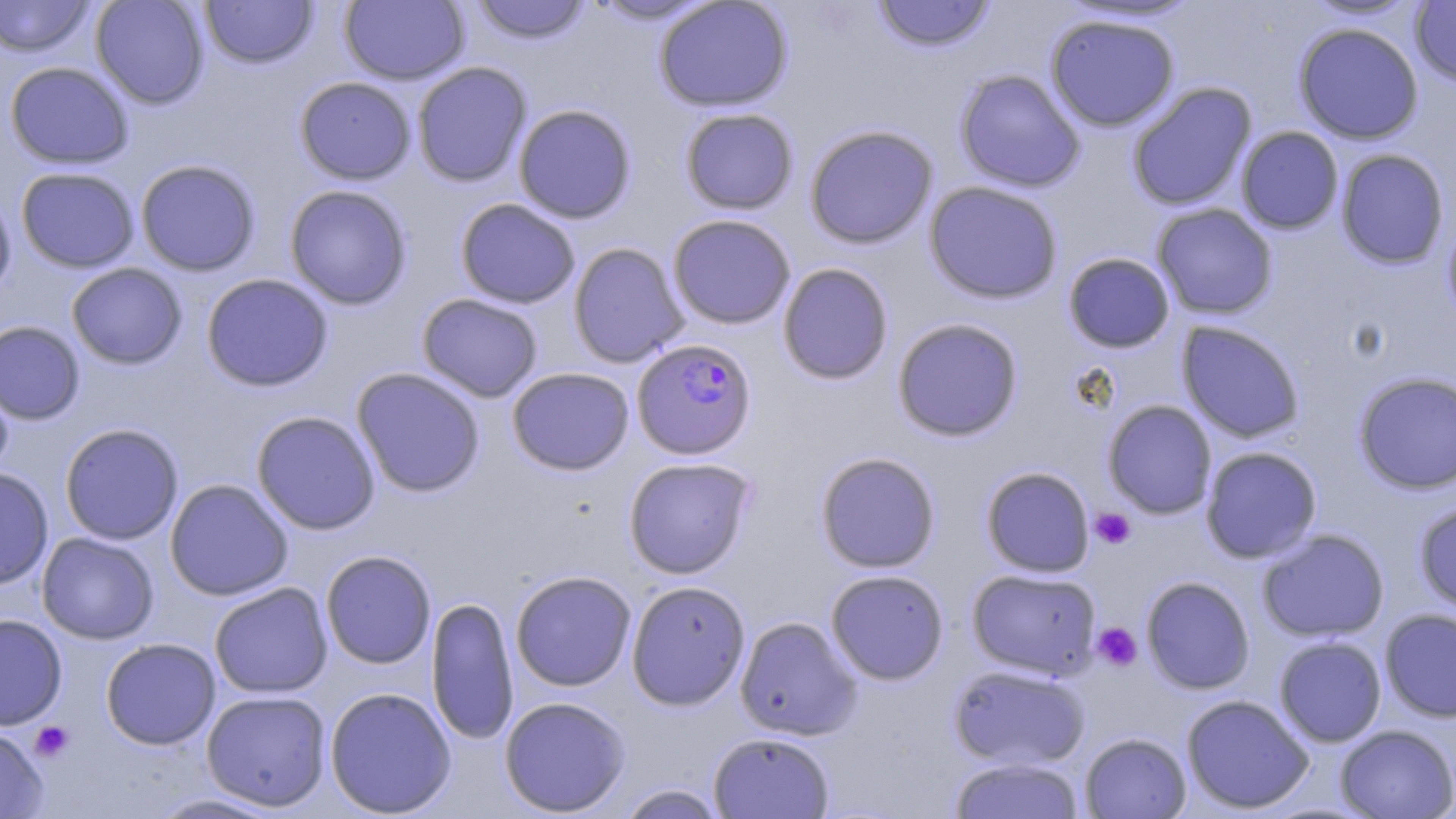
Approximate bounding boxes as (x1, y1, x2, y2) in pixels. Plasmodium falciparum-infected red blood cell locations: (627, 343, 752, 466). Uninfected red blood cell locations: (0, 0, 95, 58), (90, 0, 210, 109), (199, 0, 319, 69), (339, 0, 469, 85), (469, 0, 594, 44), (585, 0, 722, 25), (654, 0, 793, 112), (871, 0, 997, 52), (1300, 0, 1424, 22), (1409, 2, 1456, 87), (1044, 12, 1180, 132), (1293, 22, 1424, 144), (4, 61, 134, 169), (412, 61, 532, 188), (954, 69, 1086, 192), (294, 76, 417, 185), (1127, 81, 1257, 211), (513, 104, 637, 223), (680, 107, 799, 214), (804, 124, 938, 249), (1236, 126, 1343, 234), (1335, 148, 1450, 270), (135, 159, 261, 276), (16, 167, 140, 273), (924, 181, 1064, 304), (284, 184, 412, 310), (0, 187, 17, 302), (455, 198, 580, 309), (1151, 203, 1278, 319), (1442, 211, 1456, 329), (667, 214, 796, 329), (568, 242, 689, 367), (1062, 251, 1176, 353), (777, 262, 894, 385), (66, 263, 187, 369), (201, 273, 334, 392), (416, 293, 543, 402), (892, 317, 1024, 442), (0, 320, 85, 424), (1176, 320, 1305, 443), (1192, 322, 1313, 562), (0, 365, 15, 480), (351, 367, 486, 498), (507, 367, 634, 475), (1353, 370, 1456, 495), (1102, 400, 1217, 519), (251, 410, 381, 535), (59, 422, 184, 545), (1200, 446, 1322, 563), (815, 451, 941, 573), (623, 457, 756, 578), (980, 466, 1095, 578), (0, 467, 53, 590), (165, 478, 293, 600), (1413, 498, 1456, 614), (1257, 528, 1390, 643), (36, 532, 159, 645), (320, 550, 436, 669), (966, 568, 1102, 679), (825, 569, 949, 685), (510, 570, 637, 691), (1140, 575, 1256, 694), (626, 580, 750, 710), (209, 582, 333, 698), (426, 596, 518, 745), (1379, 608, 1456, 723), (0, 613, 68, 730), (734, 616, 862, 740), (1274, 636, 1387, 747), (100, 638, 220, 750), (948, 663, 1090, 769), (324, 686, 457, 817), (201, 690, 332, 811), (1181, 694, 1315, 814), (498, 696, 631, 816), (1334, 724, 1456, 819), (0, 725, 49, 818), (708, 731, 835, 818), (1079, 732, 1192, 818), (949, 756, 1084, 819), (615, 784, 728, 818), (146, 793, 289, 818). Platelet locations: (1090, 507, 1136, 550), (1092, 622, 1142, 671), (30, 721, 74, 762). Slide-level diagnosis: Plasmodium falciparum. Single field of view. Light microscopy. Image is 1456×819 pixels. May-Grünwald-Giemsa-stained preparation. 1000x magnification. Thin blood smear.